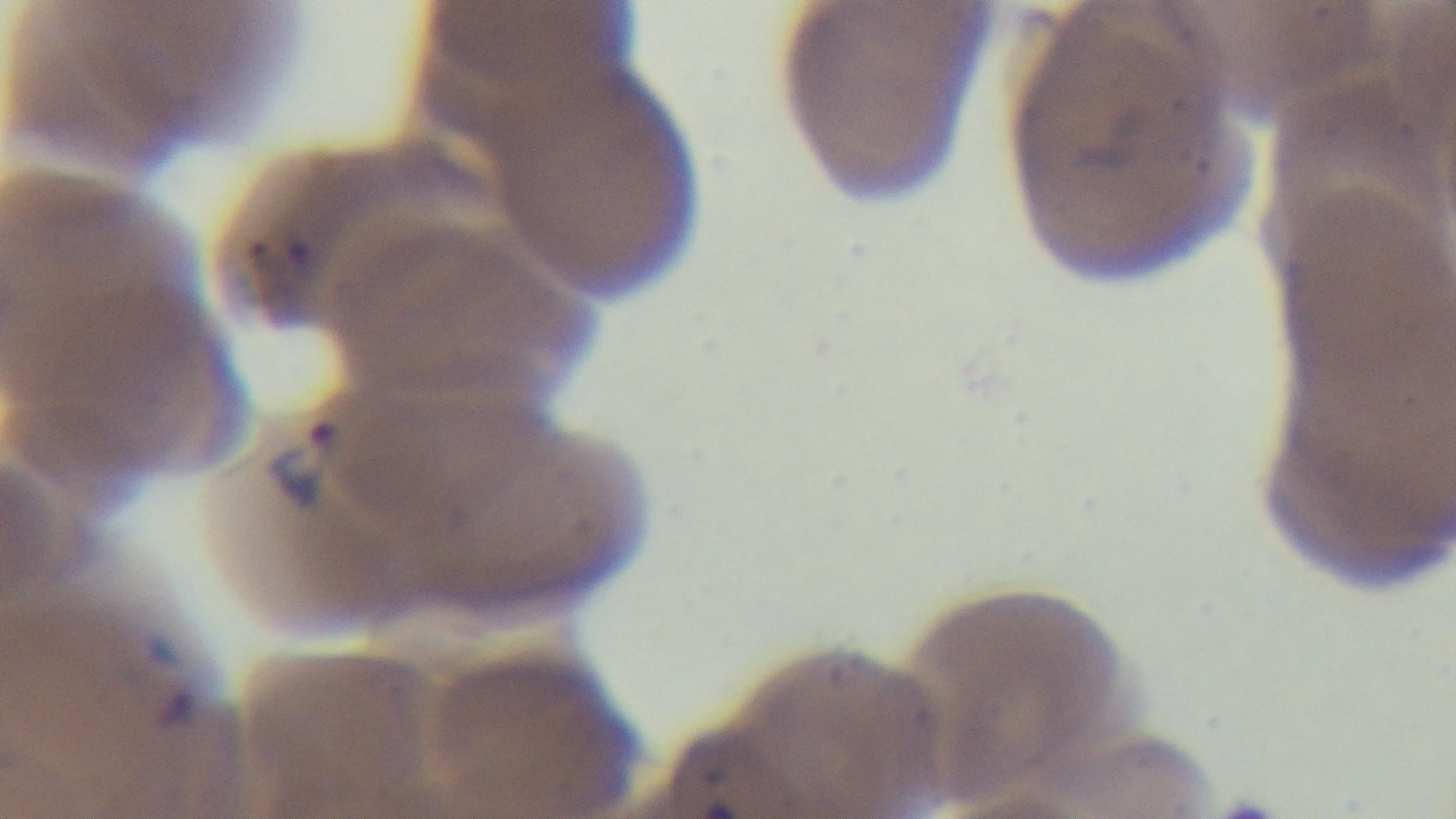
{
  "objective": "100x oil immersion",
  "capture": "mounted 4K digital camera",
  "modality": "light microscopy",
  "stain": "Giemsa",
  "field_of_view": "one from the slide",
  "malaria_status": "infected",
  "preparation": "thin smear"
}